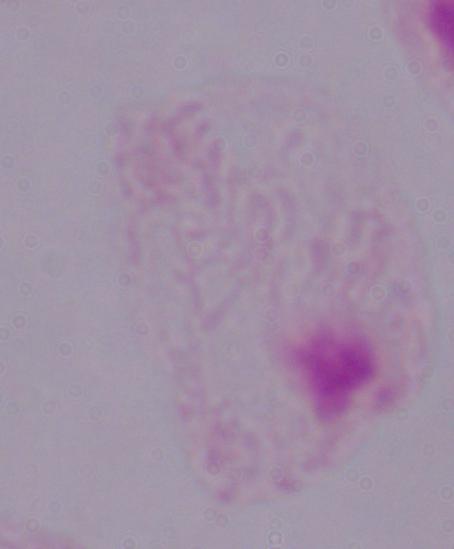

Summary:
  - Identification: trichomonad
  - Modality: photomicrograph
  - Magnification: 1000x